Report the malaria status of this cell.
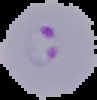
Parasitized.

From a thin blood smear. Image is 97×100 pixels. Cell region segmented out of the field of view; the surrounding area is masked to black.